State the blood parasite species.
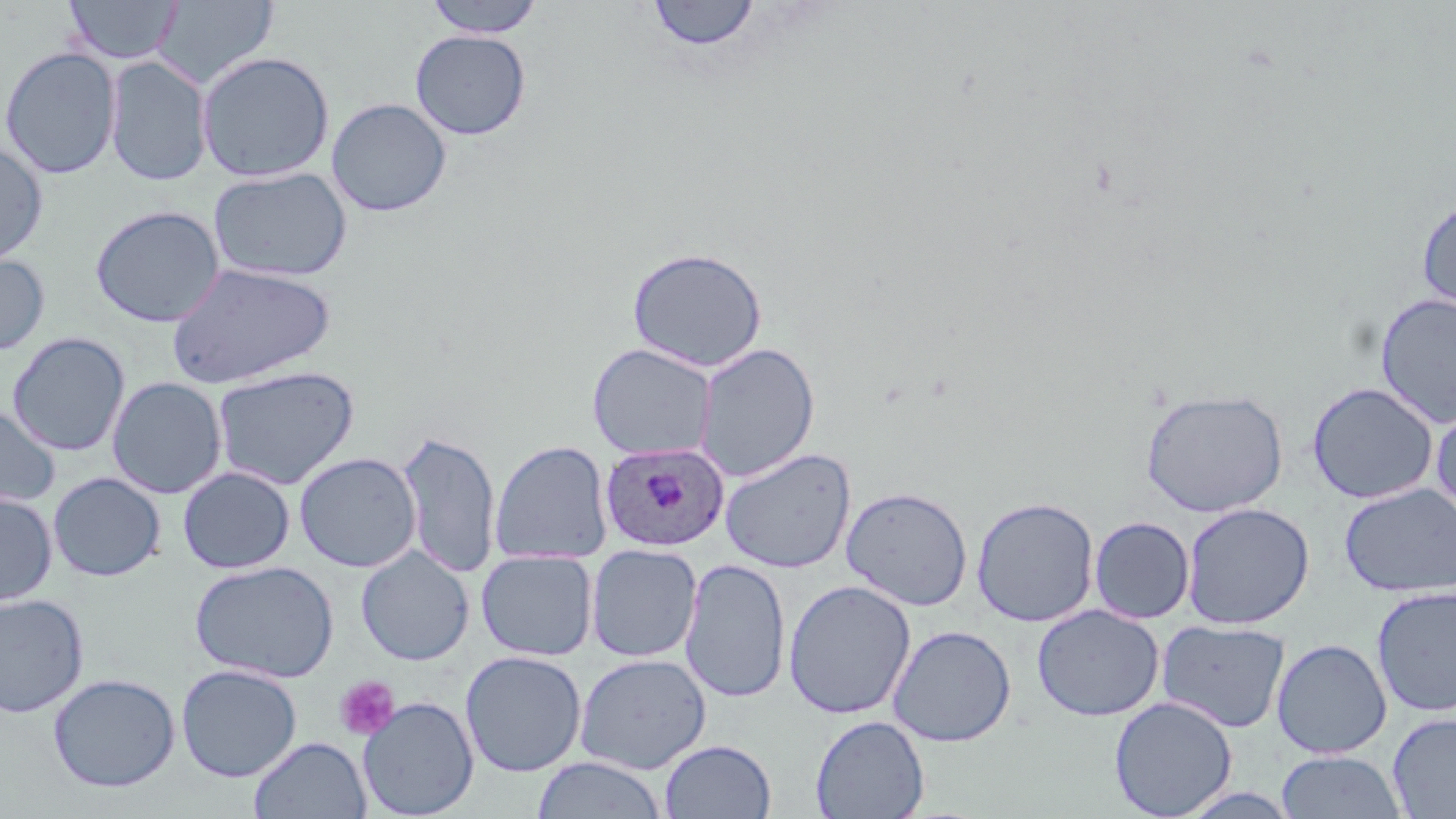
Plasmodium ovale.

Summary:
  - Coordinate format: approximate bounding boxes as (x1, y1, x2, y2) in pixels
  - Uninfected red blood cell locations: (63, 0, 183, 65), (423, 0, 546, 38), (152, 1, 278, 90), (647, 1, 761, 51), (410, 29, 531, 140), (0, 46, 121, 180), (197, 51, 335, 182), (104, 56, 213, 187), (326, 98, 452, 217), (0, 141, 48, 267), (208, 166, 352, 282), (1416, 197, 1456, 318), (90, 205, 225, 327), (627, 246, 767, 373), (0, 251, 50, 357), (166, 262, 336, 390), (1374, 291, 1456, 430), (7, 332, 130, 457), (695, 342, 820, 482), (588, 343, 717, 461), (212, 366, 359, 489), (107, 377, 227, 499), (1307, 382, 1438, 504), (1140, 388, 1289, 517), (1431, 403, 1456, 521), (0, 405, 60, 512), (397, 428, 500, 578), (490, 439, 613, 566), (720, 448, 856, 574), (295, 452, 420, 572), (177, 466, 295, 574), (48, 472, 165, 581), (1339, 483, 1456, 598), (841, 486, 973, 611), (0, 493, 57, 606), (971, 496, 1099, 627), (1181, 502, 1314, 630), (1089, 516, 1195, 623), (586, 544, 702, 663), (356, 547, 474, 665), (476, 551, 597, 661), (680, 557, 791, 703), (189, 560, 339, 683), (783, 579, 916, 720), (1371, 585, 1456, 717), (0, 593, 88, 718), (1032, 604, 1164, 722), (1156, 619, 1290, 733), (888, 625, 1016, 746), (1271, 638, 1392, 758), (460, 651, 586, 777), (575, 653, 711, 774), (176, 664, 302, 782), (48, 673, 180, 792), (1109, 696, 1237, 818), (358, 697, 478, 818), (1387, 712, 1456, 818), (810, 715, 929, 819), (250, 736, 371, 819), (659, 739, 776, 818), (1275, 751, 1407, 818), (531, 756, 668, 818)
  - Platelet locations: (334, 675, 399, 740)
  - Plasmodium ovale-infected red blood cell locations: (600, 441, 729, 552)
  - Preparation: thin blood film
  - Modality: light microscopy
  - Image size: 1456×819 pixels
  - Field of view: single
  - Magnification: 1000x
  - Stain: May-Grünwald-Giemsa